Locate and identify every blood parasite.
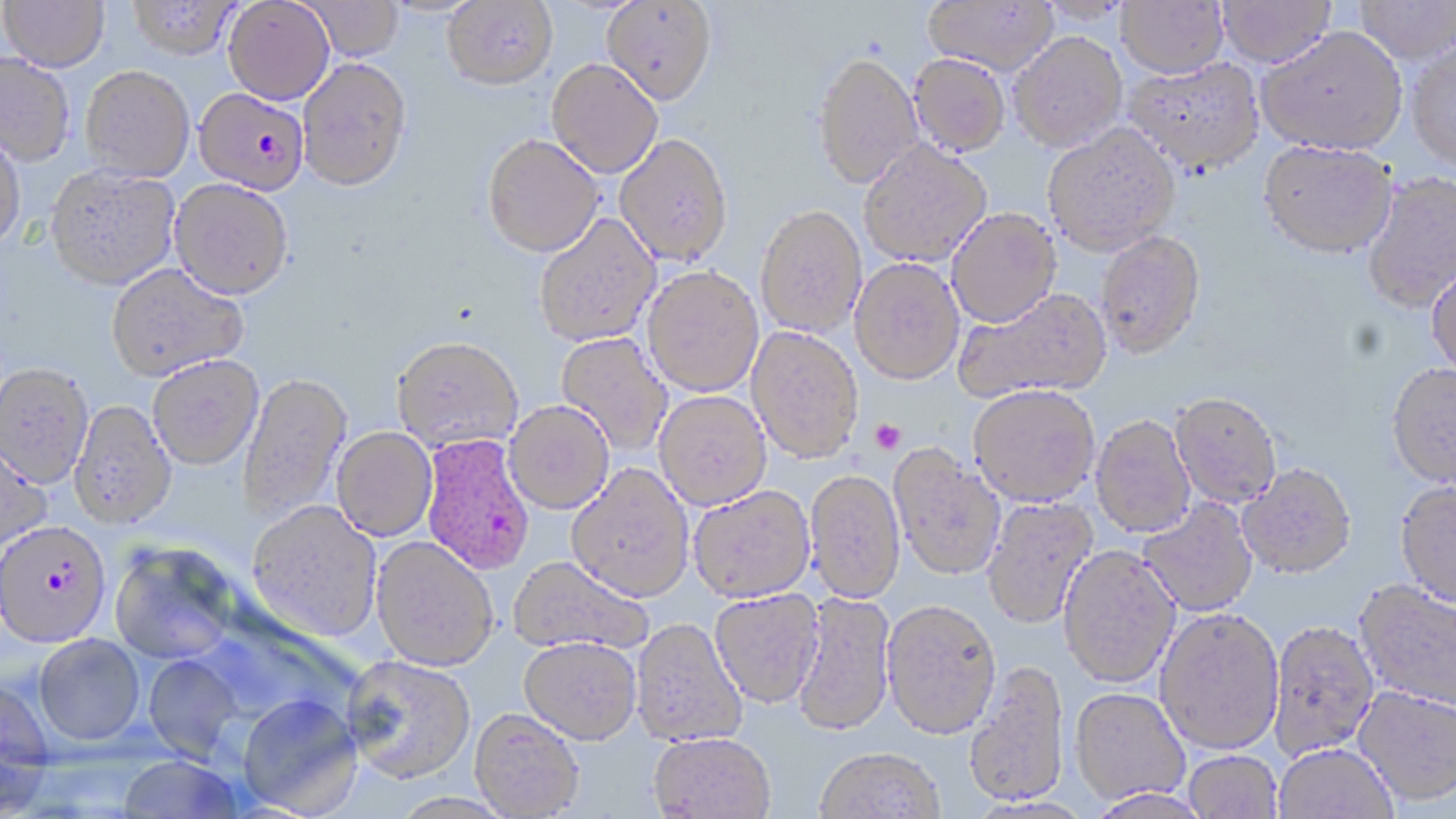
Approximate bounding boxes as named x1/y1/x2/y2 corners in pixels.
Plasmodium falciparum-infected red blood cells: (x1=193, y1=87, x2=310, y2=195), (x1=420, y1=434, x2=535, y2=575), (x1=0, y1=524, x2=109, y2=650).
No Plasmodium ovale, Plasmodium malariae, Plasmodium vivax, Babesia divergens, or Trypanosoma brucei observed.

Uninfected red blood cell locations: (x1=1, y1=0, x2=109, y2=72), (x1=128, y1=0, x2=239, y2=61), (x1=223, y1=0, x2=334, y2=104), (x1=443, y1=0, x2=558, y2=89), (x1=602, y1=0, x2=717, y2=104), (x1=923, y1=0, x2=1058, y2=74), (x1=1217, y1=0, x2=1335, y2=67), (x1=303, y1=1, x2=404, y2=61), (x1=1037, y1=1, x2=1131, y2=25), (x1=1116, y1=1, x2=1228, y2=77), (x1=1354, y1=1, x2=1455, y2=64), (x1=1257, y1=26, x2=1407, y2=154), (x1=1009, y1=32, x2=1127, y2=152), (x1=1407, y1=42, x2=1456, y2=171), (x1=813, y1=51, x2=923, y2=188), (x1=0, y1=53, x2=75, y2=167), (x1=909, y1=54, x2=1011, y2=156), (x1=298, y1=58, x2=413, y2=192), (x1=1125, y1=58, x2=1264, y2=174), (x1=547, y1=59, x2=663, y2=178), (x1=80, y1=66, x2=195, y2=182), (x1=1042, y1=124, x2=1180, y2=256), (x1=0, y1=128, x2=26, y2=254), (x1=615, y1=133, x2=733, y2=266), (x1=482, y1=134, x2=604, y2=257), (x1=858, y1=139, x2=991, y2=267), (x1=1258, y1=140, x2=1397, y2=258), (x1=45, y1=165, x2=180, y2=292), (x1=1361, y1=172, x2=1456, y2=312), (x1=169, y1=179, x2=293, y2=301), (x1=756, y1=204, x2=867, y2=337), (x1=947, y1=207, x2=1062, y2=327), (x1=533, y1=212, x2=660, y2=347), (x1=1095, y1=230, x2=1206, y2=359), (x1=850, y1=258, x2=964, y2=384), (x1=1427, y1=262, x2=1456, y2=379), (x1=106, y1=264, x2=248, y2=383), (x1=642, y1=266, x2=764, y2=396), (x1=954, y1=287, x2=1112, y2=403), (x1=746, y1=326, x2=863, y2=464), (x1=555, y1=333, x2=672, y2=456), (x1=392, y1=336, x2=523, y2=453), (x1=147, y1=356, x2=263, y2=471), (x1=1386, y1=362, x2=1456, y2=488), (x1=0, y1=365, x2=93, y2=490), (x1=237, y1=372, x2=352, y2=525), (x1=967, y1=384, x2=1101, y2=506), (x1=655, y1=391, x2=771, y2=509), (x1=1170, y1=392, x2=1281, y2=508), (x1=504, y1=400, x2=613, y2=514), (x1=69, y1=401, x2=176, y2=532), (x1=1090, y1=414, x2=1196, y2=538), (x1=332, y1=427, x2=437, y2=541), (x1=0, y1=442, x2=52, y2=554), (x1=889, y1=446, x2=1007, y2=581), (x1=566, y1=463, x2=694, y2=602), (x1=1238, y1=464, x2=1356, y2=580), (x1=804, y1=470, x2=905, y2=603), (x1=1394, y1=481, x2=1456, y2=609), (x1=689, y1=486, x2=816, y2=603), (x1=982, y1=496, x2=1098, y2=629), (x1=1138, y1=498, x2=1259, y2=617), (x1=246, y1=502, x2=382, y2=642), (x1=371, y1=537, x2=498, y2=671), (x1=110, y1=543, x2=238, y2=666), (x1=1058, y1=546, x2=1181, y2=689), (x1=508, y1=555, x2=654, y2=656), (x1=1354, y1=579, x2=1456, y2=715), (x1=710, y1=590, x2=823, y2=709), (x1=792, y1=590, x2=896, y2=739), (x1=882, y1=600, x2=1002, y2=742), (x1=1155, y1=609, x2=1284, y2=756), (x1=194, y1=614, x2=361, y2=729), (x1=631, y1=618, x2=747, y2=748), (x1=1267, y1=621, x2=1379, y2=762), (x1=34, y1=636, x2=145, y2=748), (x1=519, y1=636, x2=642, y2=744), (x1=142, y1=654, x2=245, y2=763), (x1=342, y1=655, x2=476, y2=784), (x1=964, y1=662, x2=1069, y2=809), (x1=0, y1=679, x2=55, y2=811), (x1=1353, y1=686, x2=1456, y2=808), (x1=1069, y1=689, x2=1191, y2=806), (x1=237, y1=696, x2=364, y2=818), (x1=470, y1=709, x2=585, y2=818), (x1=648, y1=733, x2=775, y2=819), (x1=1274, y1=745, x2=1398, y2=819), (x1=814, y1=750, x2=945, y2=819), (x1=1184, y1=752, x2=1283, y2=818), (x1=117, y1=757, x2=243, y2=818), (x1=1088, y1=790, x2=1214, y2=819), (x1=392, y1=793, x2=517, y2=819). Platelet locations: (x1=870, y1=419, x2=906, y2=455). Slide-level diagnosis: Plasmodium falciparum. Captured at 1000x magnification. Image is 1456×819 pixels. May-Grünwald-Giemsa-stained preparation. Thin blood film. One field of a larger specimen. Optical microscopy.